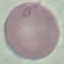
Summary:
  - Malaria status: uninfected
  - Stain: Giemsa
  - Image type: cell patch, automatically extracted from a larger field of view and resized to 64 × 64 pixels
  - Preparation: thin blood smear
  - Capture: smartphone through the microscope eyepiece